Assess the morphology of the red blood cells.
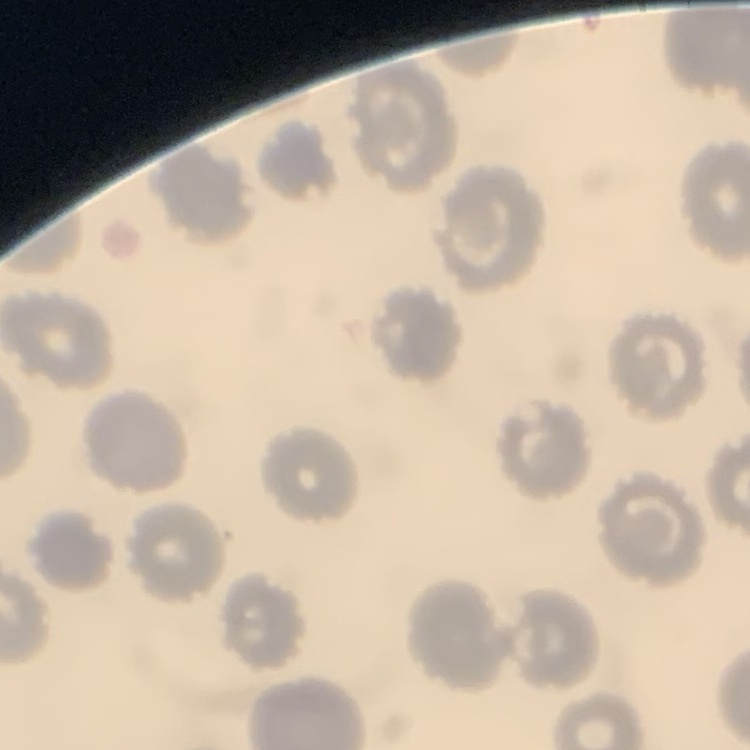

They show no rouleaux formation.

Summary:
  - Preparation: thin blood smear
  - Stain: Field's or Giemsa
  - Image type: square crop of a larger photomicrograph